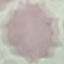

result = negative for malaria parasites
stain = Giemsa
capture = smartphone camera at the microscope eyepiece
image type = cell patch, automatically extracted from a larger field of view and resized to 64 × 64 pixels
preparation = thin blood film